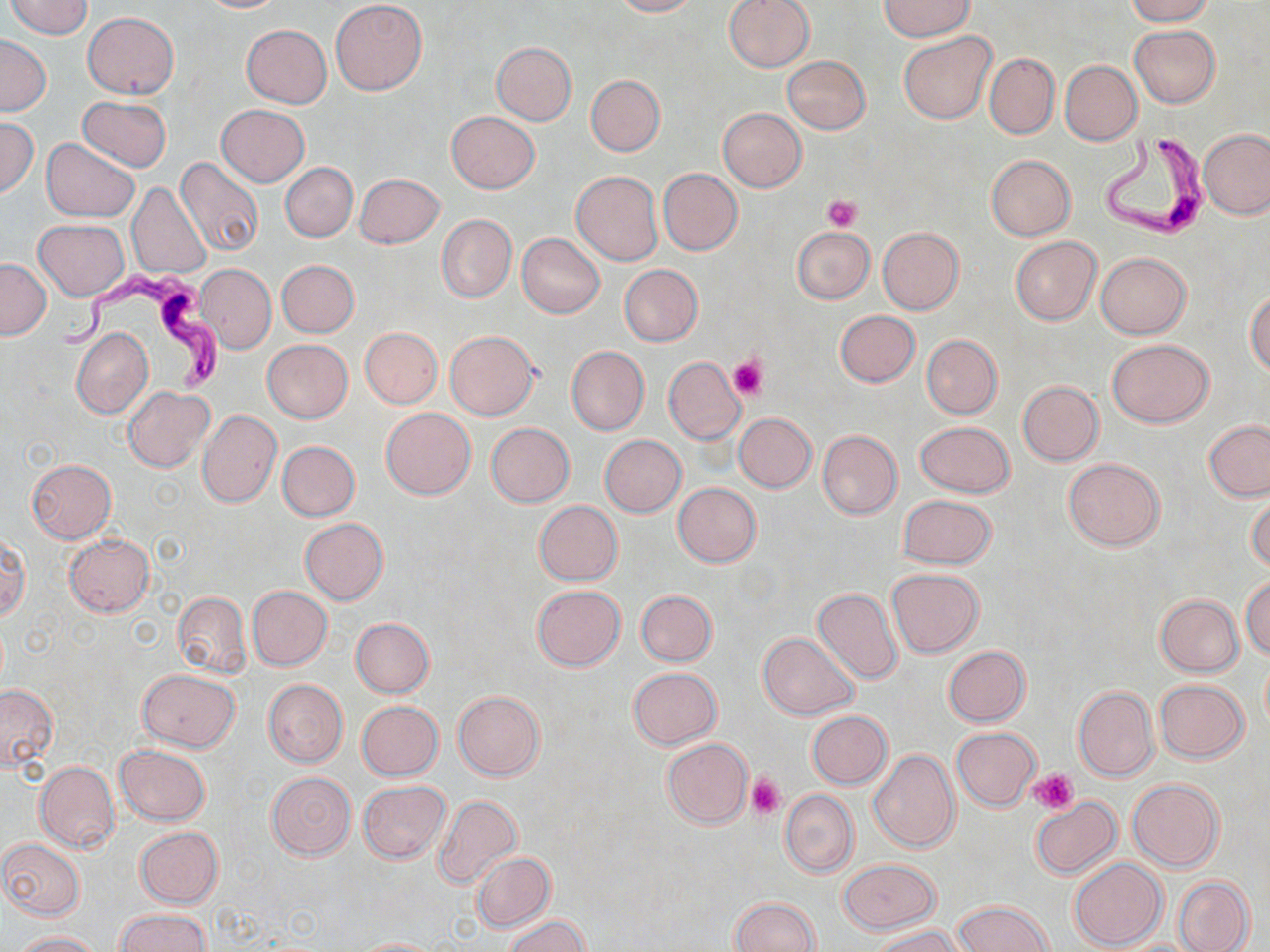 Approximate bounding boxes as (x1,y1)-(x2,y2) corner pairs in pixels. Trypanosoma brucei locations: (1099,134)-(1211,243), (55,266)-(224,397). Uninfected red blood cell locations: (4,0)-(93,38), (198,0)-(288,13), (611,0)-(699,17), (724,0)-(814,72), (1123,0)-(1216,25), (330,1)-(426,95), (879,1)-(977,42), (82,12)-(179,98), (241,24)-(331,107), (1129,25)-(1220,108), (898,31)-(997,124), (0,34)-(51,115), (491,41)-(576,125), (985,53)-(1059,138), (783,55)-(871,134), (1059,60)-(1142,145), (585,75)-(665,156), (77,96)-(171,173), (216,105)-(310,185), (718,107)-(807,192), (446,111)-(540,194), (0,117)-(39,199), (1200,129)-(1270,219), (41,138)-(139,221), (986,155)-(1076,241), (174,157)-(264,260), (280,163)-(357,241), (658,168)-(743,255), (571,171)-(662,265), (355,174)-(446,248), (126,182)-(211,279), (436,213)-(516,303), (35,219)-(129,300), (791,226)-(875,305), (878,228)-(964,313), (516,232)-(605,318), (1010,236)-(1101,325), (1095,252)-(1192,340), (0,258)-(50,339), (276,260)-(359,337), (195,263)-(275,354), (619,264)-(703,346), (1246,288)-(1270,377), (834,310)-(920,387), (72,327)-(153,419), (360,327)-(442,408), (445,330)-(540,420), (921,334)-(1002,419), (261,339)-(352,424), (1107,339)-(1214,427), (566,346)-(649,436), (663,356)-(746,444), (1017,381)-(1103,466), (123,386)-(214,472), (381,407)-(476,500), (197,410)-(281,508), (733,413)-(817,493), (1204,420)-(1270,501), (916,421)-(1015,498), (486,422)-(574,507), (817,430)-(903,518), (600,435)-(685,516), (277,440)-(360,521), (1063,458)-(1165,550), (27,459)-(115,542), (673,483)-(761,567), (1248,491)-(1270,574), (898,495)-(997,569), (533,500)-(622,586), (299,518)-(387,604), (65,534)-(154,615), (0,536)-(30,622), (886,568)-(983,658), (1241,575)-(1270,660), (531,585)-(625,671), (246,586)-(332,671), (813,587)-(902,685), (636,590)-(717,666), (171,592)-(251,678), (1154,594)-(1244,676), (351,617)-(434,697), (758,632)-(858,720), (944,645)-(1030,726), (628,667)-(722,749), (137,669)-(240,751), (263,679)-(348,767), (1155,680)-(1248,763), (0,685)-(57,771), (1073,685)-(1159,781), (454,690)-(544,780), (356,701)-(442,781), (806,710)-(892,789), (952,726)-(1039,810), (662,738)-(753,828), (114,744)-(211,825), (869,749)-(959,852), (34,761)-(119,853), (266,772)-(355,860), (1127,779)-(1222,871), (357,781)-(450,864), (780,789)-(858,877), (433,796)-(521,889), (1030,797)-(1121,878), (135,827)-(223,908), (0,838)-(85,920), (471,851)-(555,931), (838,858)-(942,934), (1069,858)-(1167,949), (1173,875)-(1254,952), (729,896)-(818,951), (953,901)-(1052,952), (115,909)-(211,952), (502,914)-(593,952), (872,925)-(966,951), (10,930)-(102,951), (352,936)-(440,951). Platelet locations: (823,195)-(862,232), (730,355)-(767,401), (1030,769)-(1079,813), (747,774)-(785,819). Slide-level diagnosis: Trypanosoma brucei. Thin blood film. Optical microscopy. May-Grünwald-Giemsa stain. 1000x magnification. Single field of view. Image is 1270×952 pixels.